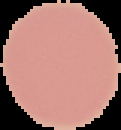
Summary:
  - Preparation: thin blood film
  - Image type: segmented cell region with the area outside set to black
  - Image size: 121×130 pixels
  - Result: no malaria parasites seen